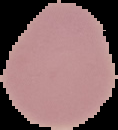 From a thin blood smear. Image is 118×130 pixels. The area outside the segmented cell region is set to black. Result: no Plasmodium parasites seen.